Give the extent of all Plasmodium falciparum-infected red blood cells.
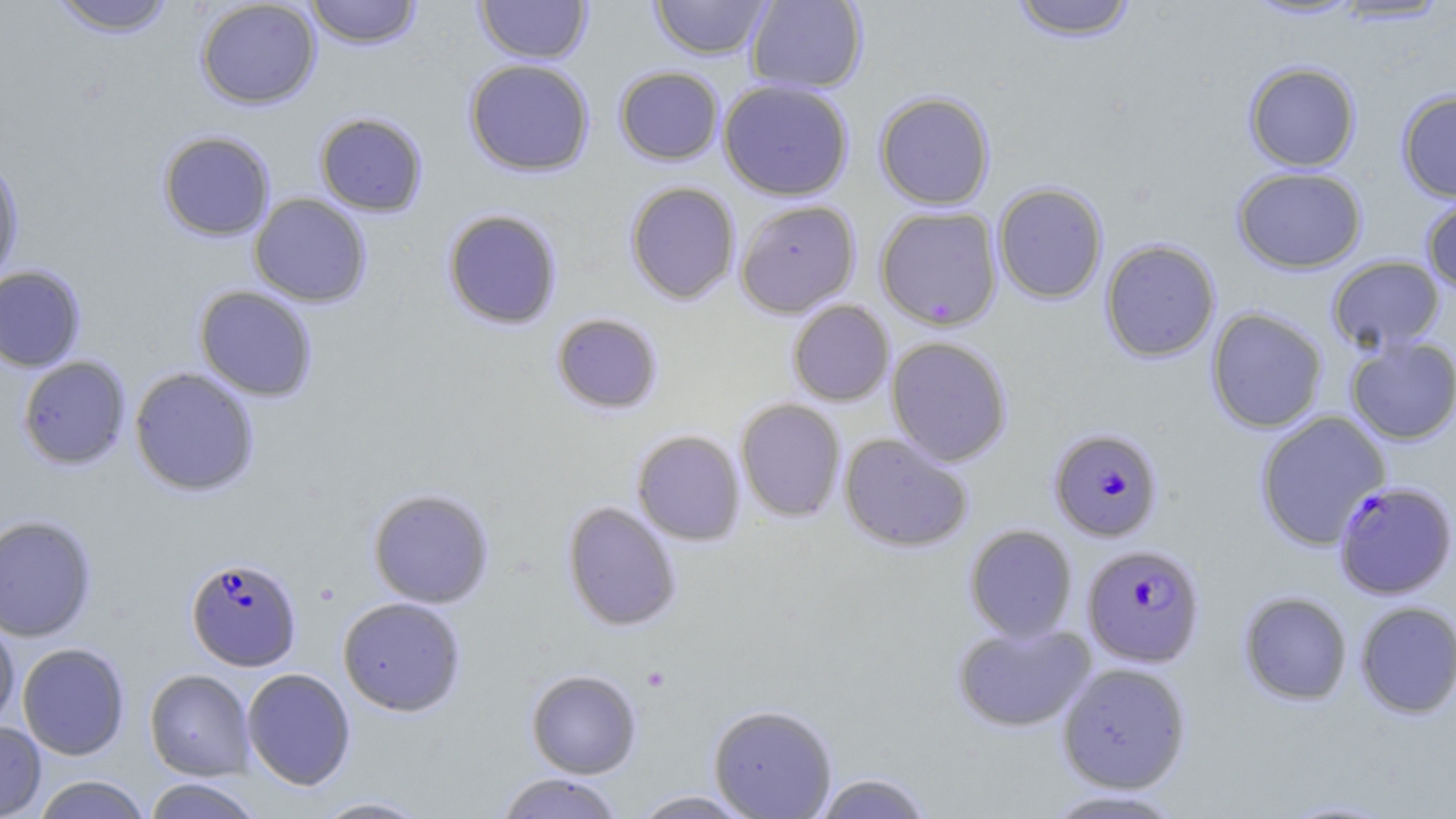

Approximate bounding boxes as (x1,y1)-(x2,y2) corner pairs in pixels.
Plasmodium falciparum-infected red blood cells: (1048,427)-(1163,541), (1333,480)-(1456,599), (1081,543)-(1205,667), (186,556)-(302,671).

Summary:
  - Platelet locations: (640,665)-(672,692)
  - Uninfected red blood cell locations: (49,0)-(177,36), (195,0)-(321,109), (304,0)-(423,49), (475,0)-(592,64), (649,0)-(774,60), (745,0)-(868,94), (1009,0)-(1139,41), (1243,0)-(1364,21), (1328,1)-(1452,26), (464,58)-(595,177), (1244,61)-(1361,172), (614,66)-(724,165), (717,79)-(854,201), (1397,90)-(1456,202), (874,91)-(995,210), (314,111)-(428,217), (157,130)-(276,241), (0,156)-(25,286), (1232,166)-(1367,273), (624,181)-(740,305), (993,182)-(1109,304), (249,193)-(372,307), (1421,196)-(1456,296), (734,199)-(861,317), (875,205)-(1003,331), (442,208)-(563,330), (1099,238)-(1221,363), (1327,255)-(1445,353), (0,265)-(87,372), (194,285)-(318,401), (787,300)-(894,406), (1206,307)-(1328,434), (551,312)-(664,415), (886,336)-(1013,466), (1345,336)-(1456,444), (17,356)-(131,470), (129,366)-(260,497), (734,398)-(846,522), (1254,410)-(1391,550), (631,430)-(745,546), (839,432)-(973,553), (367,488)-(495,609), (562,501)-(681,632), (0,514)-(98,642), (964,524)-(1078,642), (1239,591)-(1352,705), (337,596)-(467,716), (1355,601)-(1456,719), (0,615)-(20,731), (952,622)-(1095,732), (17,642)-(130,760), (1056,662)-(1192,793), (241,668)-(356,790), (145,669)-(255,780), (526,669)-(642,778), (709,703)-(837,818), (0,720)-(46,818), (494,772)-(625,819), (811,772)-(936,818), (32,775)-(151,819), (142,778)-(265,819), (1037,789)-(1189,818), (629,790)-(759,818), (309,796)-(433,818), (1274,797)-(1405,818)
  - Slide-level diagnosis: Plasmodium falciparum
  - Field of view: one of a larger specimen
  - Modality: optical microscopy
  - Magnification: 1000x
  - Image size: 1456×819 pixels
  - Stain: May-Grünwald-Giemsa
  - Preparation: thin blood smear